Locate and identify every blood parasite.
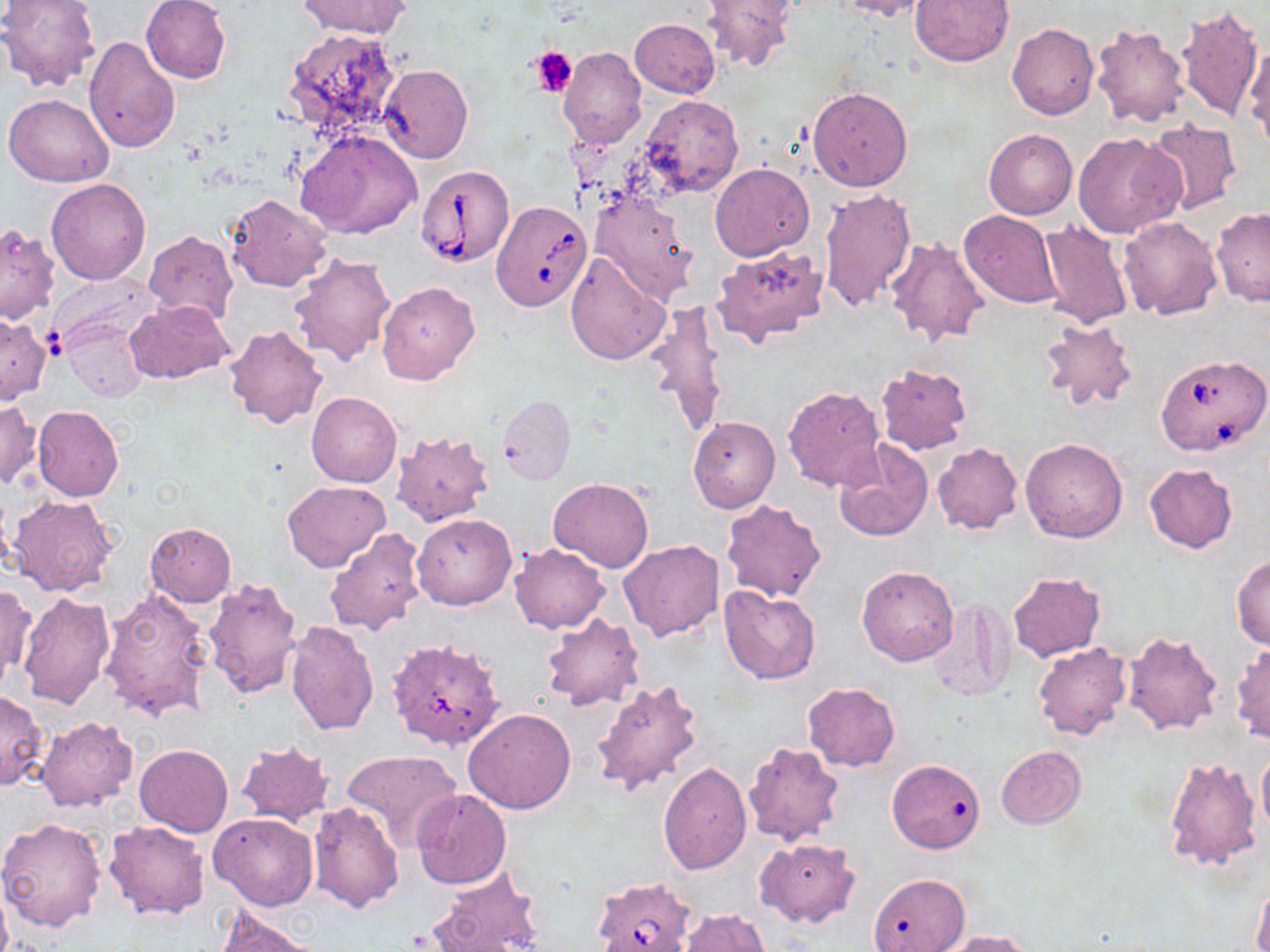
Approximate bounding boxes as named x1/y1/x2/y2 corners in pixels.
Babesia divergens-infected red blood cells: (x1=416, y1=164, x2=514, y2=267), (x1=492, y1=200, x2=592, y2=311), (x1=1154, y1=354, x2=1270, y2=457), (x1=591, y1=878, x2=698, y2=952).
No Plasmodium falciparum, Plasmodium ovale, Plasmodium malariae, Plasmodium vivax, or Trypanosoma brucei observed.

Uninfected red blood cell locations: (x1=140, y1=0, x2=232, y2=85), (x1=297, y1=0, x2=411, y2=39), (x1=700, y1=0, x2=797, y2=72), (x1=837, y1=0, x2=932, y2=21), (x1=909, y1=0, x2=1014, y2=67), (x1=0, y1=1, x2=101, y2=93), (x1=1176, y1=3, x2=1263, y2=123), (x1=634, y1=10, x2=793, y2=85), (x1=629, y1=19, x2=720, y2=98), (x1=1089, y1=22, x2=1190, y2=128), (x1=1007, y1=23, x2=1098, y2=120), (x1=282, y1=28, x2=403, y2=139), (x1=84, y1=36, x2=180, y2=155), (x1=1243, y1=38, x2=1270, y2=149), (x1=557, y1=46, x2=646, y2=149), (x1=378, y1=64, x2=472, y2=164), (x1=807, y1=85, x2=914, y2=192), (x1=4, y1=93, x2=114, y2=186), (x1=641, y1=95, x2=743, y2=198), (x1=1144, y1=120, x2=1242, y2=215), (x1=297, y1=129, x2=421, y2=240), (x1=984, y1=129, x2=1077, y2=219), (x1=1075, y1=132, x2=1184, y2=238), (x1=709, y1=163, x2=814, y2=261), (x1=46, y1=179, x2=151, y2=285), (x1=818, y1=188, x2=916, y2=312), (x1=589, y1=190, x2=697, y2=304), (x1=227, y1=193, x2=333, y2=293), (x1=1211, y1=207, x2=1269, y2=306), (x1=959, y1=210, x2=1060, y2=308), (x1=1118, y1=215, x2=1221, y2=319), (x1=1036, y1=219, x2=1135, y2=331), (x1=0, y1=223, x2=60, y2=323), (x1=144, y1=232, x2=238, y2=326), (x1=885, y1=237, x2=989, y2=346), (x1=710, y1=243, x2=829, y2=347), (x1=565, y1=250, x2=670, y2=366), (x1=289, y1=253, x2=396, y2=367), (x1=48, y1=272, x2=160, y2=354), (x1=377, y1=282, x2=480, y2=385), (x1=124, y1=300, x2=234, y2=385), (x1=646, y1=303, x2=728, y2=438), (x1=0, y1=314, x2=51, y2=405), (x1=1037, y1=316, x2=1138, y2=411), (x1=63, y1=322, x2=149, y2=403), (x1=223, y1=324, x2=328, y2=429), (x1=876, y1=362, x2=973, y2=455), (x1=782, y1=385, x2=886, y2=491), (x1=306, y1=392, x2=401, y2=487), (x1=498, y1=395, x2=574, y2=485), (x1=0, y1=400, x2=41, y2=489), (x1=32, y1=406, x2=124, y2=501), (x1=687, y1=416, x2=780, y2=513), (x1=391, y1=431, x2=495, y2=526), (x1=1020, y1=436, x2=1129, y2=542), (x1=833, y1=441, x2=934, y2=541), (x1=932, y1=443, x2=1022, y2=534), (x1=1144, y1=462, x2=1238, y2=553), (x1=548, y1=477, x2=654, y2=573), (x1=283, y1=480, x2=390, y2=572), (x1=8, y1=494, x2=118, y2=598), (x1=720, y1=499, x2=826, y2=602), (x1=412, y1=514, x2=516, y2=610), (x1=145, y1=523, x2=236, y2=606), (x1=325, y1=528, x2=428, y2=637), (x1=617, y1=540, x2=725, y2=642), (x1=509, y1=543, x2=608, y2=634), (x1=1232, y1=552, x2=1270, y2=650), (x1=857, y1=565, x2=958, y2=666), (x1=1007, y1=572, x2=1104, y2=660), (x1=201, y1=578, x2=303, y2=702), (x1=0, y1=582, x2=36, y2=691), (x1=719, y1=585, x2=822, y2=684), (x1=99, y1=589, x2=214, y2=721), (x1=17, y1=591, x2=116, y2=713), (x1=923, y1=599, x2=1015, y2=701), (x1=541, y1=612, x2=644, y2=712), (x1=285, y1=620, x2=380, y2=735), (x1=1123, y1=630, x2=1223, y2=736), (x1=1231, y1=641, x2=1270, y2=744), (x1=1032, y1=643, x2=1133, y2=742), (x1=391, y1=646, x2=509, y2=750), (x1=591, y1=676, x2=705, y2=797), (x1=803, y1=682, x2=899, y2=770), (x1=0, y1=691, x2=48, y2=789), (x1=462, y1=707, x2=576, y2=814), (x1=37, y1=716, x2=138, y2=813), (x1=742, y1=740, x2=846, y2=847), (x1=236, y1=741, x2=336, y2=828), (x1=134, y1=743, x2=233, y2=836), (x1=996, y1=745, x2=1085, y2=828), (x1=1257, y1=745, x2=1270, y2=842), (x1=341, y1=748, x2=460, y2=851), (x1=1162, y1=756, x2=1262, y2=871), (x1=658, y1=762, x2=752, y2=874), (x1=889, y1=764, x2=979, y2=857), (x1=412, y1=788, x2=512, y2=889), (x1=309, y1=802, x2=404, y2=912), (x1=208, y1=812, x2=318, y2=911), (x1=0, y1=817, x2=107, y2=933), (x1=103, y1=820, x2=209, y2=920), (x1=756, y1=838, x2=859, y2=928), (x1=429, y1=867, x2=545, y2=952), (x1=872, y1=871, x2=972, y2=952), (x1=0, y1=880, x2=12, y2=952), (x1=1253, y1=882, x2=1270, y2=952), (x1=213, y1=904, x2=319, y2=952), (x1=677, y1=910, x2=772, y2=952), (x1=945, y1=930, x2=1037, y2=952). Platelet locations: (x1=531, y1=45, x2=578, y2=97). Slide-level diagnosis: Babesia divergens. Image is 1270×952 pixels. Light microscopy. One field of a larger specimen. 1000x magnification. May-Grünwald-Giemsa-stained preparation. Thin blood smear.